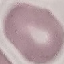

Summary:
  - Result: no malaria parasites seen
  - Capture: smartphone camera at the microscope eyepiece
  - Stain: Giemsa
  - Preparation: thin smear
  - Image type: automatically extracted cell patch, resized to 64 × 64 pixels